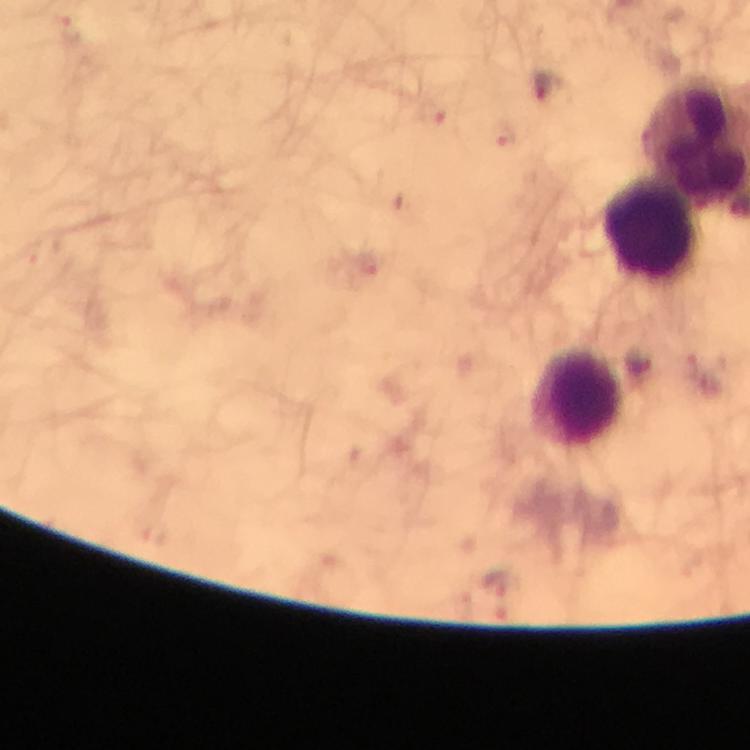
Approximate centers as {x, y} in pixels.
Summary:
  - Leukocyte locations: {656, 229}, {580, 399}
  - Malaria parasite locations: {68, 29}, {548, 86}, {434, 112}, {502, 140}, {369, 268}, {687, 370}, {640, 371}
  - Immersion oil: applied
  - Cropped from: a single field of view
  - Context: from a malaria diagnostic workup
  - Preparation: thick blood smear
  - Capture: smartphone mounted on the microscope
  - Stain: Giemsa
  - Image size: 750×750 pixels
  - Magnification: 100x